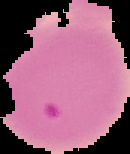

Image is 130×154 pixels. From a thin blood smear. Result: malaria parasites detected. Segmented cell region on a black background.